Locate every blood parasite and identify its species.
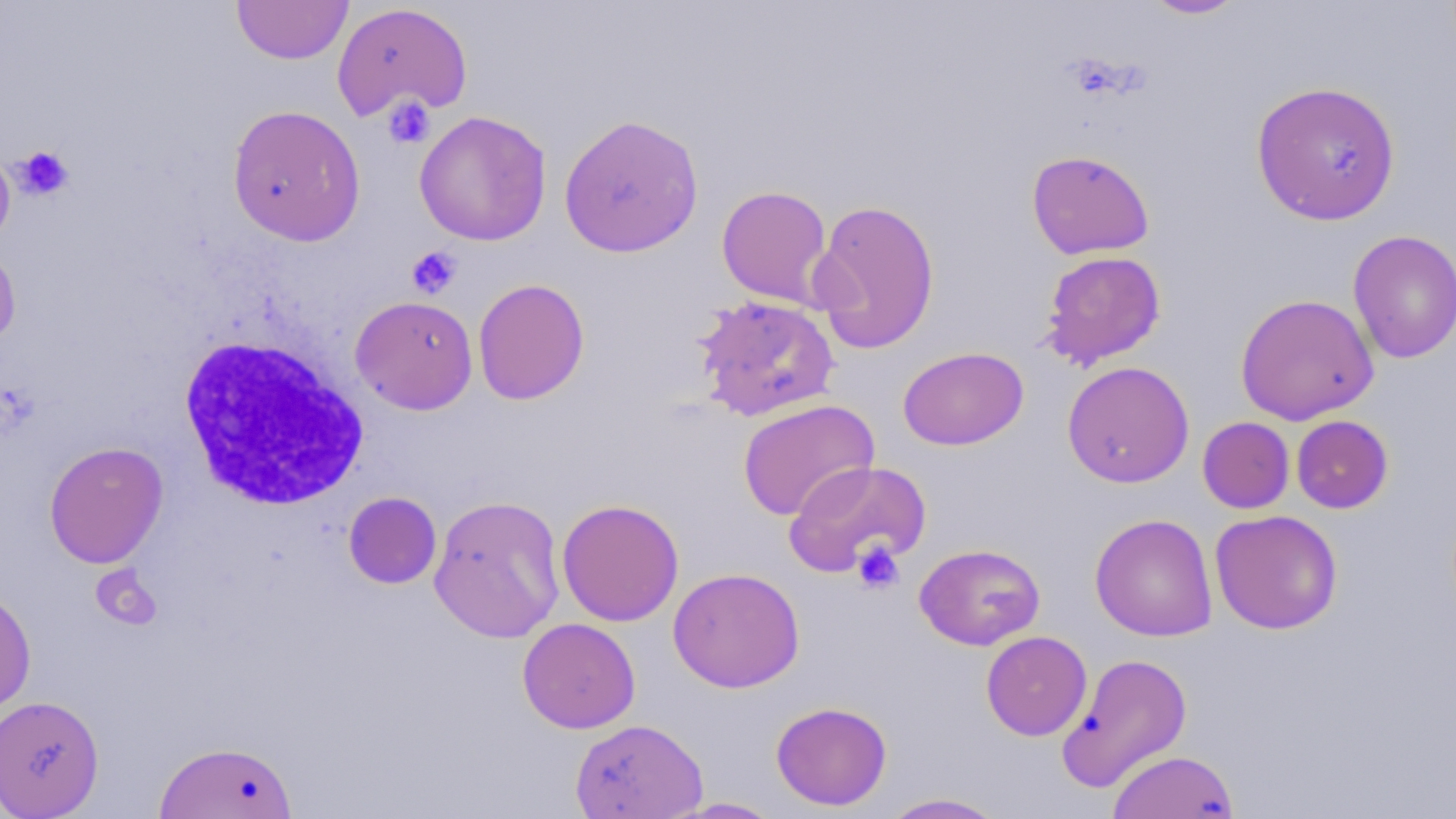

No blood parasites seen.

{
  "slide_level_diagnosis": "negative for blood parasites",
  "uninfected_red_blood_cell_locations": "approximate bounding boxes as (x1, y1, x2, y2) in pixels: (231, 0, 353, 64), (1140, 0, 1248, 20), (331, 3, 472, 121), (1251, 80, 1401, 226), (226, 104, 366, 246), (414, 110, 552, 246), (559, 113, 703, 258), (0, 146, 15, 249), (1026, 150, 1154, 260), (716, 185, 833, 308), (809, 199, 941, 354), (1347, 230, 1456, 363), (0, 243, 21, 352), (1039, 250, 1167, 370), (472, 278, 590, 405), (1235, 293, 1378, 425), (692, 294, 840, 423), (350, 295, 478, 415), (897, 347, 1028, 450), (1061, 360, 1194, 488), (737, 399, 879, 521), (1291, 415, 1393, 513), (1198, 416, 1295, 514), (44, 441, 168, 568), (784, 460, 932, 577), (343, 491, 442, 589), (427, 494, 566, 642), (556, 498, 685, 626), (1209, 509, 1343, 634), (1089, 513, 1218, 641), (914, 543, 1045, 650), (668, 567, 805, 692), (0, 585, 37, 719), (517, 617, 641, 733), (980, 631, 1092, 741), (1056, 651, 1194, 793), (0, 694, 105, 818), (771, 701, 892, 810), (570, 718, 708, 819), (153, 740, 298, 818), (1107, 749, 1239, 818), (880, 793, 1008, 818), (661, 797, 785, 818)",
  "magnification": "1000x",
  "modality": "light microscopy",
  "stain": "May-Grünwald-Giemsa",
  "preparation": "thin blood film",
  "white_blood_cell_locations": "approximate bounding boxes as (x1, y1, x2, y2) in pixels: (178, 335, 369, 511)",
  "field_of_view": "one of a larger specimen",
  "platelet_locations": "approximate bounding boxes as (x1, y1, x2, y2) in pixels: (382, 95, 436, 149), (1321, 133, 1369, 179), (12, 145, 75, 201), (406, 246, 462, 299), (851, 540, 904, 594), (91, 565, 163, 632)",
  "image_size": "1456×819 pixels"
}